Mark where platelets are.
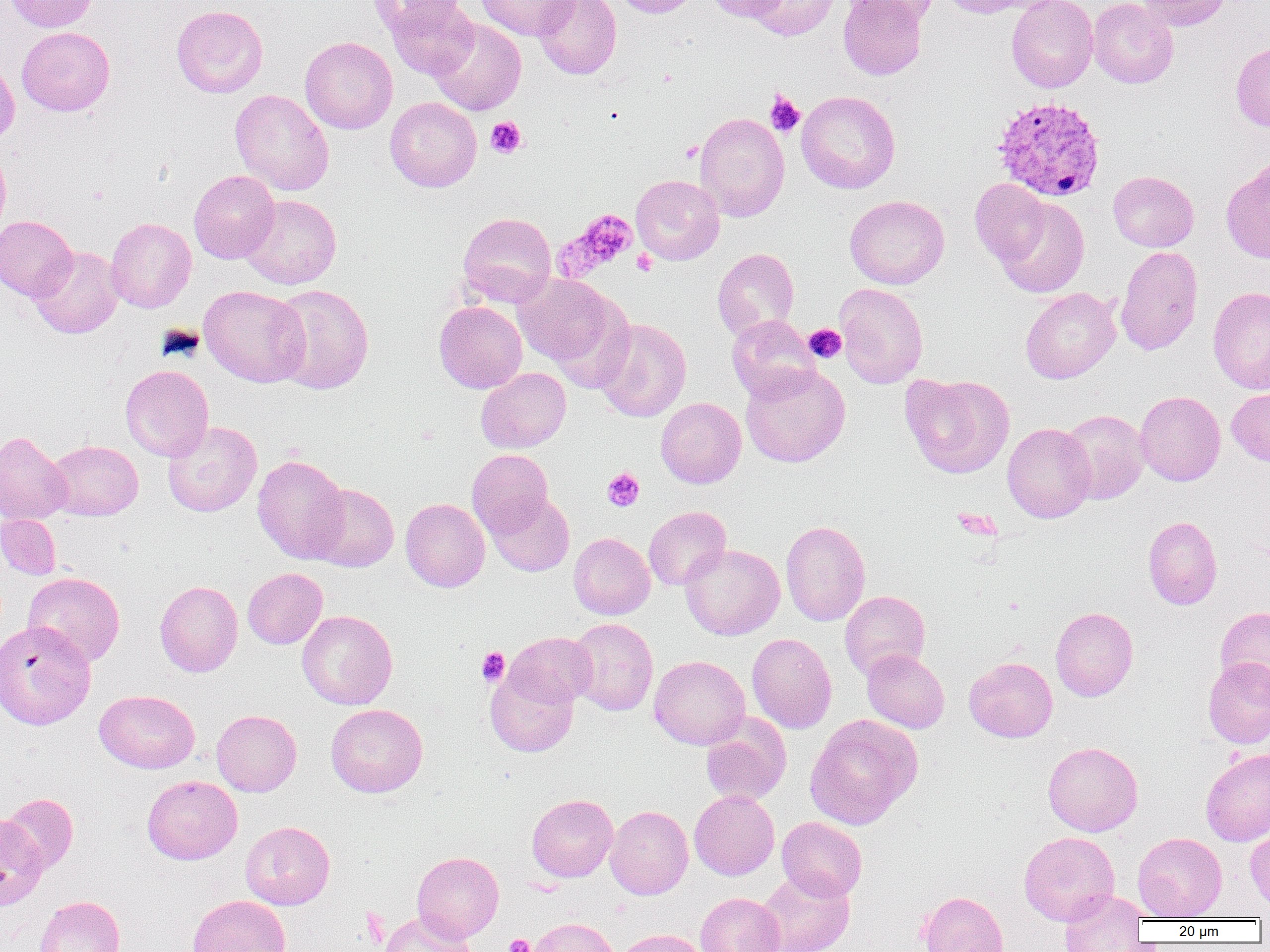
Approximate bounding boxes as [x1, y1, x2, y2] in pixels.
Platelets: [765, 92, 804, 136], [485, 117, 527, 158], [680, 141, 703, 162], [557, 209, 639, 279], [632, 249, 657, 276], [804, 324, 846, 363], [602, 468, 644, 512], [952, 506, 1000, 541], [477, 647, 509, 686], [505, 933, 534, 952].

Uninfected red blood cell locations: [5, 0, 100, 32], [368, 0, 465, 38], [383, 0, 479, 79], [475, 0, 578, 41], [533, 0, 622, 79], [611, 0, 700, 17], [703, 0, 788, 21], [745, 0, 840, 40], [838, 0, 926, 80], [846, 0, 940, 24], [940, 0, 1041, 18], [1006, 0, 1098, 93], [1087, 0, 1178, 88], [1135, 0, 1231, 31], [171, 5, 268, 98], [429, 17, 526, 116], [17, 27, 115, 116], [299, 36, 398, 134], [1231, 41, 1270, 132], [0, 58, 19, 147], [230, 89, 334, 196], [796, 90, 900, 194], [385, 97, 482, 192], [694, 111, 789, 221], [0, 146, 11, 240], [1221, 160, 1270, 263], [188, 170, 279, 263], [1108, 171, 1199, 252], [631, 175, 724, 265], [970, 179, 1051, 267], [239, 194, 341, 289], [845, 195, 949, 289], [994, 197, 1090, 298], [457, 212, 556, 307], [0, 215, 78, 301], [106, 217, 196, 313], [29, 245, 124, 339], [1116, 246, 1203, 356], [712, 248, 800, 340], [514, 274, 621, 369], [271, 283, 374, 394], [834, 283, 928, 388], [199, 285, 309, 387], [1208, 286, 1270, 394], [1020, 287, 1121, 384], [434, 301, 527, 393], [727, 314, 820, 403], [594, 318, 691, 422], [740, 363, 850, 467], [120, 364, 214, 461], [476, 367, 571, 453], [901, 373, 1015, 479], [1227, 388, 1270, 466], [1134, 391, 1225, 486], [656, 397, 746, 488], [1060, 409, 1150, 504], [162, 420, 262, 517], [1002, 423, 1096, 523], [0, 430, 71, 525], [46, 440, 143, 521], [467, 449, 554, 538], [252, 454, 350, 563], [308, 483, 399, 572], [485, 493, 574, 576], [400, 498, 490, 592], [643, 506, 731, 590], [0, 514, 61, 579], [1143, 516, 1222, 610], [780, 519, 871, 626], [568, 532, 655, 619], [680, 543, 785, 640], [243, 568, 327, 648], [23, 571, 125, 666], [155, 580, 243, 677], [839, 590, 930, 680], [1215, 606, 1270, 695], [1051, 607, 1138, 701], [297, 610, 397, 709], [568, 618, 658, 716], [0, 619, 96, 730], [505, 632, 597, 709], [747, 633, 837, 733], [862, 649, 949, 733], [649, 655, 750, 750], [964, 657, 1057, 742], [1203, 657, 1270, 748], [485, 667, 579, 757], [94, 690, 200, 773], [325, 703, 428, 797], [211, 709, 301, 796], [805, 714, 922, 830], [700, 715, 791, 806], [1043, 742, 1143, 836], [1201, 748, 1270, 846], [142, 775, 242, 865], [689, 789, 779, 880], [1, 793, 79, 874], [527, 794, 618, 882], [605, 805, 693, 899], [0, 815, 47, 910], [776, 816, 867, 902], [241, 821, 335, 910], [1245, 827, 1270, 911], [1019, 831, 1119, 925], [1132, 832, 1227, 920], [412, 851, 504, 942], [756, 869, 855, 952], [1059, 889, 1148, 951], [918, 890, 1008, 952], [695, 892, 785, 952], [188, 894, 291, 952], [35, 895, 124, 952], [379, 911, 477, 952], [526, 918, 618, 952], [615, 928, 709, 952]. Plasmodium vivax-infected red blood cell locations: [992, 96, 1107, 202]. Slide-level diagnosis: Plasmodium vivax. Single field of view. Optical microscopy. Thin blood smear. Captured at 1000x magnification. Image is 1270×952 pixels.